Give the extent of all Babesia divergens-infected red blood cells.
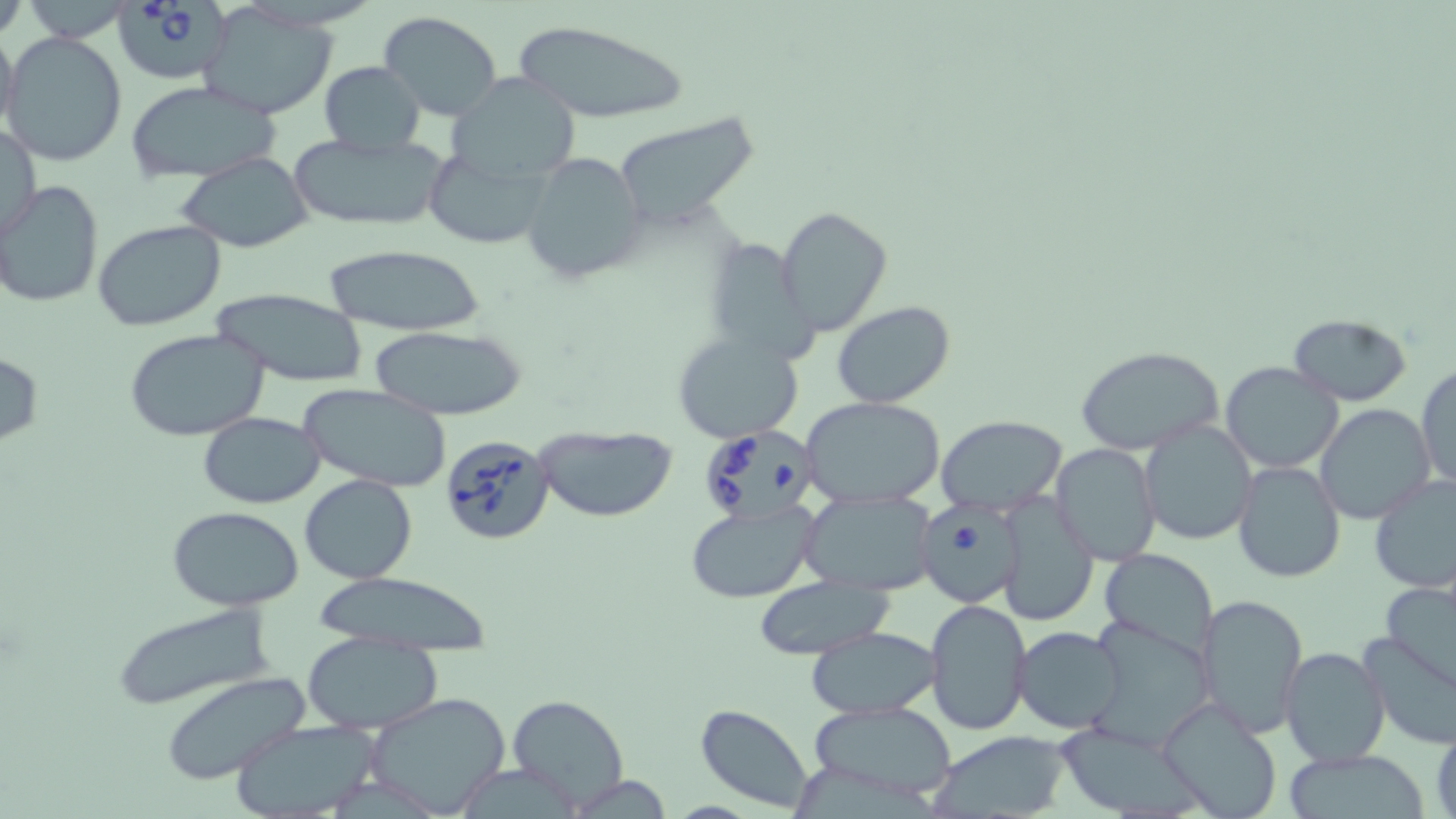
Approximate bounding boxes as [x1, y1, x2, y2] in pixels.
Babesia divergens-infected red blood cells: [116, 0, 230, 79], [702, 425, 824, 530], [441, 434, 556, 545], [913, 504, 1025, 607].

Uninfected red blood cell locations: [204, 6, 338, 119], [378, 11, 504, 122], [0, 20, 20, 143], [511, 22, 690, 126], [3, 30, 129, 166], [319, 61, 424, 153], [447, 71, 583, 187], [125, 81, 283, 183], [611, 113, 762, 228], [2, 120, 41, 244], [289, 132, 450, 231], [433, 152, 564, 251], [522, 152, 648, 285], [176, 153, 314, 252], [1, 181, 103, 309], [774, 205, 892, 338], [91, 219, 227, 331], [707, 240, 826, 367], [322, 244, 487, 337], [208, 288, 370, 386], [833, 301, 956, 410], [1287, 314, 1415, 405], [367, 326, 527, 418], [125, 328, 270, 442], [672, 331, 805, 442], [1077, 345, 1225, 457], [0, 352, 43, 445], [1219, 361, 1345, 474], [1415, 362, 1455, 492], [299, 383, 452, 492], [802, 395, 947, 507], [1315, 403, 1436, 526], [197, 413, 328, 507], [937, 414, 1067, 516], [1139, 421, 1256, 547], [533, 424, 678, 524], [1050, 443, 1162, 567], [1233, 461, 1345, 583], [299, 475, 417, 585], [1369, 475, 1456, 592], [798, 491, 939, 595], [995, 493, 1098, 626], [685, 503, 817, 601], [168, 506, 305, 611], [1098, 548, 1218, 657], [309, 572, 497, 652], [755, 577, 891, 659], [1379, 580, 1456, 693], [1196, 593, 1308, 737], [923, 598, 1032, 738], [111, 605, 277, 713], [1086, 618, 1217, 748], [1012, 625, 1129, 733], [804, 626, 946, 719], [1358, 630, 1456, 749], [301, 635, 445, 731], [1280, 646, 1389, 767], [160, 673, 312, 786], [364, 692, 513, 818], [506, 694, 629, 811], [1159, 698, 1284, 819], [807, 700, 959, 804], [696, 704, 816, 815], [230, 719, 383, 819], [1430, 719, 1456, 819], [1054, 720, 1211, 819], [928, 730, 1069, 817], [1281, 751, 1437, 819]. Slide-level diagnosis: Babesia divergens. Thin blood film. Optical microscopy. May-Grünwald-Giemsa stain. Captured at 1000x magnification. Image is 1456×819 pixels. One field of a larger specimen.